Find each WBC.
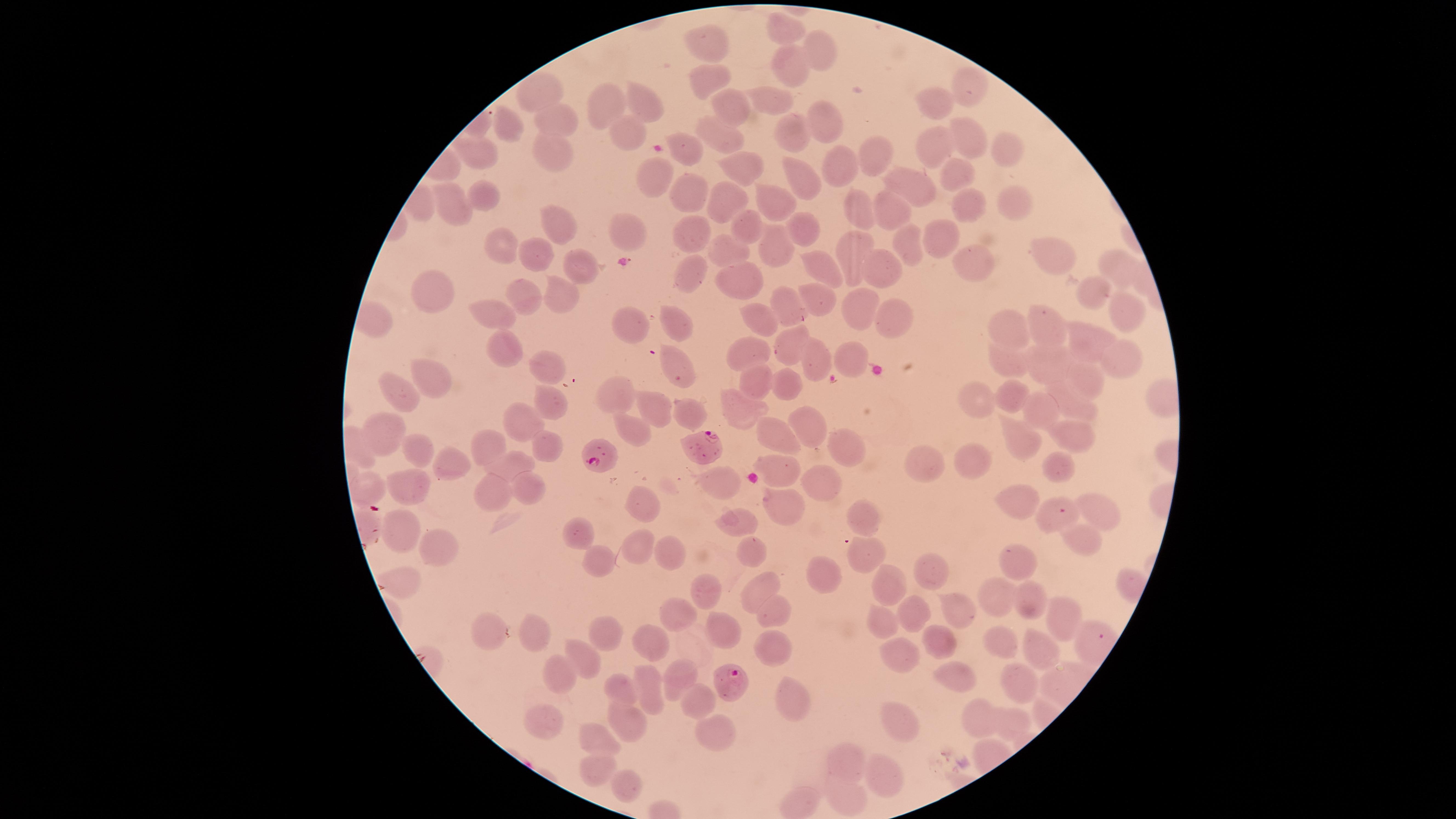

No WBCs identified.

Approximate marker points as (x, y) in pixels. Uninfected RBCs: (785, 31), (707, 43), (816, 54), (789, 66), (706, 81), (972, 89), (536, 90), (772, 98), (606, 103), (647, 103), (732, 105), (935, 107), (548, 116), (823, 123), (509, 128), (718, 134), (968, 135), (621, 136), (790, 136), (1006, 147), (929, 148), (688, 151), (562, 154), (470, 155), (876, 155), (744, 164), (844, 170), (952, 172), (655, 176), (798, 176), (905, 185), (685, 189), (485, 193), (727, 200), (768, 201), (448, 205), (1012, 205), (964, 209), (890, 211), (862, 213), (748, 222), (561, 226), (620, 228), (808, 231), (692, 235), (938, 240), (508, 245), (910, 245), (774, 247), (853, 249), (535, 252), (730, 252), (1049, 253), (968, 265), (1116, 265), (580, 266), (878, 268), (824, 270), (690, 272), (735, 272), (1096, 294), (437, 295), (532, 298), (820, 299), (562, 300), (788, 307), (852, 311), (1120, 311), (891, 316), (498, 317), (763, 320), (671, 323), (631, 326), (1048, 330), (1008, 331), (1084, 340), (787, 344), (501, 347), (751, 354), (844, 359), (1046, 359), (1123, 360), (816, 361), (545, 362), (677, 364), (1009, 366), (756, 378), (1083, 383), (788, 384), (433, 385), (612, 391), (1008, 395), (403, 397), (977, 402), (1067, 402), (550, 405), (655, 409), (733, 409), (685, 412), (1042, 416), (803, 419), (524, 421), (632, 425), (383, 426), (1021, 436), (776, 437), (1074, 440), (839, 445), (494, 447), (546, 447), (421, 451), (516, 464), (979, 465), (921, 466), (454, 467), (780, 467), (1059, 468), (719, 482), (815, 482), (411, 485), (521, 486), (491, 487), (373, 488), (1017, 501), (780, 506), (644, 507), (1101, 509), (736, 517), (1050, 519), (864, 522), (397, 526), (582, 536), (1081, 539), (641, 547), (433, 548), (750, 551), (865, 551), (670, 557), (1015, 560), (599, 562), (925, 571), (828, 576), (888, 579), (402, 581), (762, 588), (993, 589), (701, 591), (1021, 601), (912, 608), (1057, 611), (769, 615), (881, 615), (959, 616), (678, 617), (603, 629), (720, 629), (537, 637), (494, 638), (651, 641), (934, 641), (999, 641), (770, 645), (1043, 650), (898, 655), (579, 660), (959, 672), (564, 675), (680, 676), (1017, 680), (625, 691), (654, 692), (698, 704), (793, 705), (544, 719), (904, 720), (981, 721), (631, 722), (1009, 723), (591, 736), (716, 737), (849, 764), (597, 766), (886, 774), (624, 778), (838, 798). Parasitized RBCs: (708, 450), (604, 452), (730, 678). One field of view of the specimen. Thin blood smear. Image is 1456×819 pixels. Species: Plasmodium falciparum. Circular visible region. Smartphone photograph through the microscope eyepiece. Giemsa-stained preparation. Presence: malaria parasites identified.